Report the malaria status of this cell.
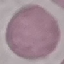
Uninfected.

Summary:
  - Preparation: thin smear
  - Capture: smartphone camera at the microscope eyepiece
  - Stain: Giemsa
  - Image type: automatically extracted cell patch, resized to 64 × 64 pixels